Comment on the morphology of the erythrocytes.
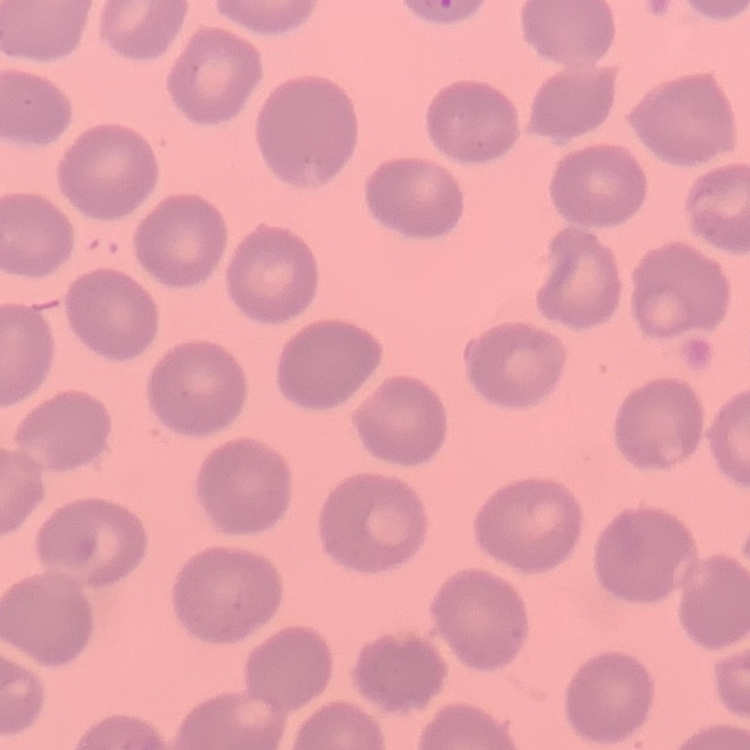
No rouleaux formation.

Thin peripheral smear. Stained with either Field's or Giemsa. One tile cut from a larger photomicrograph.